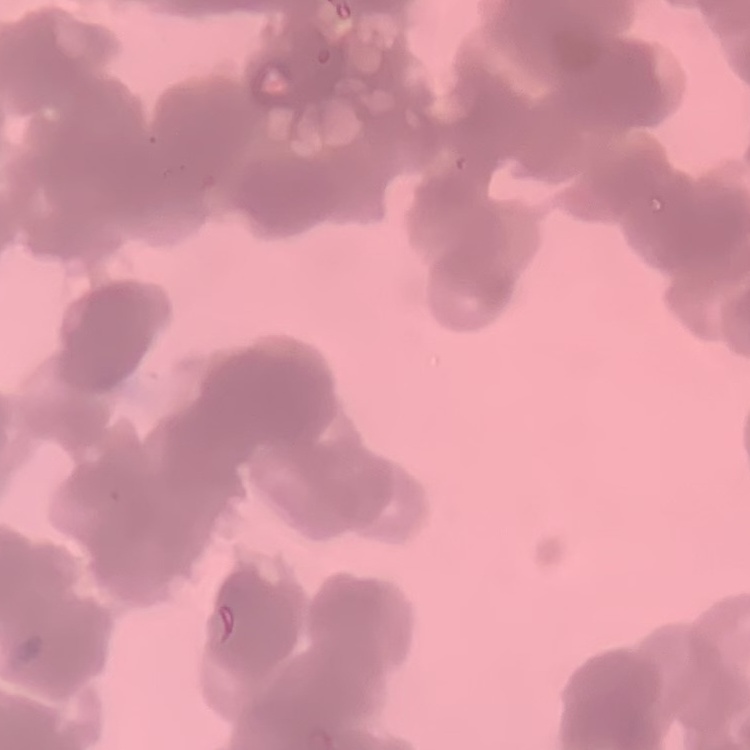

The erythrocytes show rouleaux formation. Stained with either Field's or Giemsa. Thin blood smear. One tile cut from a larger photomicrograph.